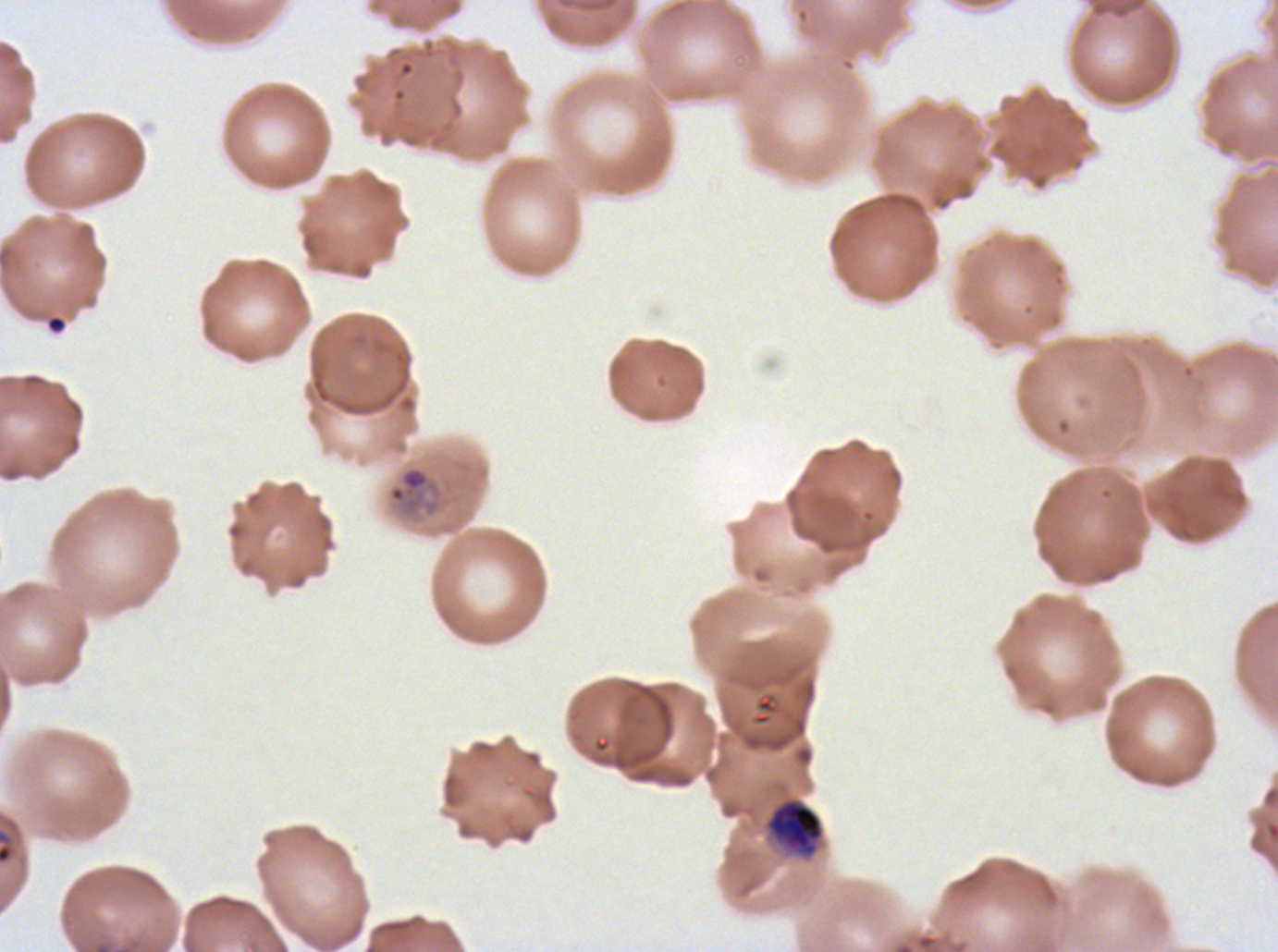
Approximate bounding boxes as {x1, y1, x2, y2} in pixels.
Summary:
  - Early schizont locations: {767, 799, 824, 856}
  - Debris locations: {46, 315, 67, 333}
  - Mid trophozoite locations: {387, 466, 442, 517}
  - Preparation: thin blood film
  - Life-cycle stages observed: mid trophozoite, early schizont
  - Field of view: sub-image separated from a larger composite
  - Stain: Giemsa
  - Image size: 1278×952 pixels
  - Specimen: Plasmodium falciparum from a patient in The Gambia, cultured ex vivo for 24 to 48 hours